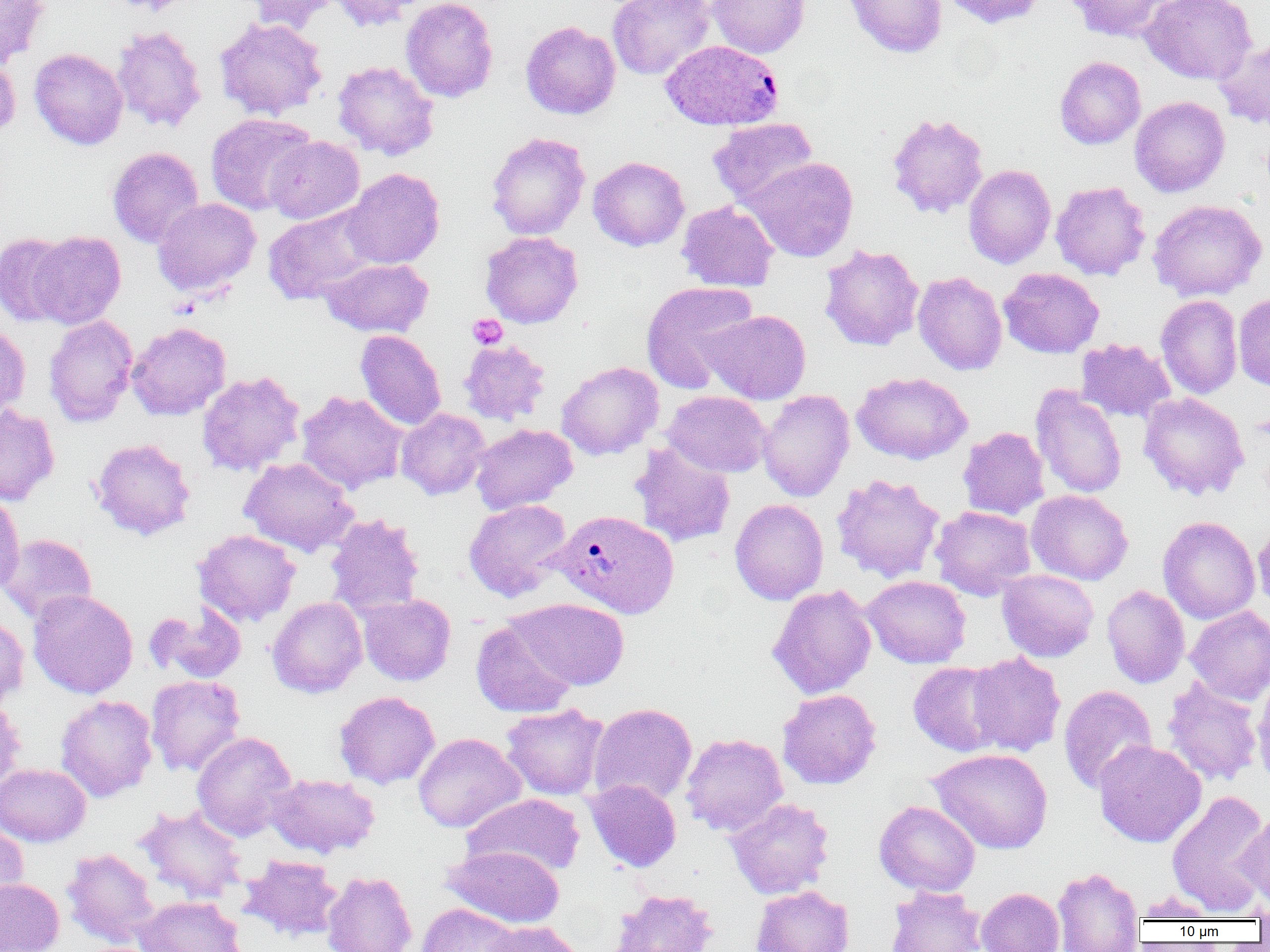
Approximate bounding boxes as named x1/y1/x2/y2 corners in pixels. Uninfected red blood cell locations: (x1=0, y1=0, x2=49, y2=67), (x1=108, y1=0, x2=196, y2=15), (x1=239, y1=0, x2=343, y2=33), (x1=327, y1=0, x2=424, y2=31), (x1=401, y1=0, x2=498, y2=103), (x1=607, y1=0, x2=715, y2=80), (x1=707, y1=0, x2=810, y2=58), (x1=843, y1=0, x2=947, y2=58), (x1=940, y1=0, x2=1047, y2=29), (x1=1064, y1=0, x2=1177, y2=42), (x1=1140, y1=0, x2=1257, y2=85), (x1=214, y1=17, x2=328, y2=120), (x1=520, y1=21, x2=621, y2=119), (x1=112, y1=25, x2=207, y2=133), (x1=1212, y1=36, x2=1270, y2=130), (x1=29, y1=48, x2=128, y2=150), (x1=0, y1=52, x2=20, y2=140), (x1=1054, y1=56, x2=1145, y2=149), (x1=332, y1=60, x2=439, y2=160), (x1=1129, y1=96, x2=1230, y2=197), (x1=886, y1=112, x2=989, y2=218), (x1=205, y1=113, x2=316, y2=216), (x1=708, y1=118, x2=818, y2=207), (x1=486, y1=132, x2=590, y2=240), (x1=265, y1=136, x2=364, y2=224), (x1=107, y1=147, x2=205, y2=248), (x1=588, y1=156, x2=689, y2=251), (x1=742, y1=157, x2=859, y2=262), (x1=963, y1=164, x2=1056, y2=268), (x1=342, y1=168, x2=444, y2=269), (x1=1051, y1=181, x2=1151, y2=280), (x1=153, y1=198, x2=261, y2=296), (x1=668, y1=199, x2=770, y2=388), (x1=1148, y1=199, x2=1267, y2=301), (x1=676, y1=200, x2=779, y2=292), (x1=263, y1=204, x2=381, y2=304), (x1=26, y1=230, x2=126, y2=328), (x1=480, y1=231, x2=584, y2=328), (x1=0, y1=232, x2=74, y2=327), (x1=819, y1=244, x2=924, y2=351), (x1=320, y1=258, x2=433, y2=337), (x1=998, y1=267, x2=1104, y2=358), (x1=912, y1=271, x2=1007, y2=375), (x1=641, y1=281, x2=758, y2=392), (x1=1233, y1=293, x2=1270, y2=392), (x1=1156, y1=294, x2=1243, y2=399), (x1=704, y1=309, x2=811, y2=404), (x1=44, y1=315, x2=138, y2=427), (x1=0, y1=322, x2=30, y2=421), (x1=127, y1=322, x2=231, y2=420), (x1=355, y1=330, x2=446, y2=431), (x1=1076, y1=338, x2=1175, y2=423), (x1=458, y1=339, x2=550, y2=425), (x1=556, y1=361, x2=664, y2=460), (x1=197, y1=371, x2=305, y2=475), (x1=852, y1=372, x2=972, y2=465), (x1=1030, y1=384, x2=1127, y2=498), (x1=758, y1=389, x2=855, y2=502), (x1=296, y1=390, x2=408, y2=494), (x1=663, y1=390, x2=771, y2=477), (x1=1139, y1=392, x2=1249, y2=500), (x1=0, y1=404, x2=59, y2=505), (x1=396, y1=408, x2=490, y2=500), (x1=470, y1=423, x2=577, y2=514), (x1=957, y1=427, x2=1050, y2=520), (x1=91, y1=438, x2=196, y2=541), (x1=630, y1=442, x2=737, y2=548), (x1=239, y1=457, x2=359, y2=557), (x1=830, y1=473, x2=946, y2=583), (x1=1026, y1=489, x2=1133, y2=585), (x1=0, y1=490, x2=25, y2=596), (x1=730, y1=498, x2=828, y2=605), (x1=463, y1=499, x2=573, y2=602), (x1=930, y1=506, x2=1036, y2=600), (x1=325, y1=514, x2=425, y2=616), (x1=1158, y1=516, x2=1261, y2=624), (x1=1253, y1=523, x2=1270, y2=614), (x1=193, y1=529, x2=301, y2=627), (x1=0, y1=533, x2=97, y2=624), (x1=997, y1=569, x2=1098, y2=662), (x1=862, y1=575, x2=971, y2=668), (x1=767, y1=585, x2=877, y2=699), (x1=1101, y1=585, x2=1190, y2=688), (x1=27, y1=590, x2=138, y2=699), (x1=358, y1=593, x2=456, y2=685), (x1=267, y1=596, x2=367, y2=698), (x1=509, y1=598, x2=630, y2=690), (x1=147, y1=603, x2=247, y2=683), (x1=1186, y1=605, x2=1270, y2=704), (x1=0, y1=614, x2=30, y2=708), (x1=471, y1=620, x2=578, y2=718), (x1=964, y1=652, x2=1066, y2=757), (x1=908, y1=661, x2=1008, y2=757), (x1=146, y1=675, x2=245, y2=776), (x1=1161, y1=676, x2=1264, y2=787), (x1=1252, y1=678, x2=1270, y2=789), (x1=1058, y1=684, x2=1158, y2=795), (x1=777, y1=689, x2=882, y2=789), (x1=334, y1=691, x2=440, y2=789), (x1=55, y1=694, x2=157, y2=802), (x1=0, y1=696, x2=26, y2=794), (x1=500, y1=703, x2=609, y2=800), (x1=588, y1=703, x2=697, y2=806), (x1=192, y1=731, x2=297, y2=841), (x1=413, y1=732, x2=526, y2=833), (x1=680, y1=733, x2=788, y2=836), (x1=1094, y1=739, x2=1207, y2=848), (x1=927, y1=747, x2=1053, y2=854), (x1=0, y1=763, x2=91, y2=847), (x1=266, y1=773, x2=380, y2=858), (x1=584, y1=779, x2=682, y2=872), (x1=1166, y1=789, x2=1270, y2=915), (x1=463, y1=792, x2=584, y2=879), (x1=725, y1=798, x2=834, y2=899), (x1=874, y1=800, x2=980, y2=896), (x1=135, y1=804, x2=248, y2=903), (x1=1238, y1=807, x2=1270, y2=912), (x1=0, y1=823, x2=28, y2=914), (x1=444, y1=844, x2=565, y2=929), (x1=61, y1=848, x2=159, y2=948), (x1=238, y1=854, x2=344, y2=942), (x1=1052, y1=866, x2=1145, y2=952), (x1=321, y1=870, x2=417, y2=952), (x1=0, y1=878, x2=64, y2=952), (x1=751, y1=885, x2=854, y2=952), (x1=886, y1=886, x2=986, y2=952), (x1=976, y1=887, x2=1064, y2=952), (x1=609, y1=888, x2=718, y2=952), (x1=1133, y1=892, x2=1220, y2=922), (x1=132, y1=895, x2=246, y2=952), (x1=1245, y1=897, x2=1270, y2=923), (x1=417, y1=903, x2=520, y2=952), (x1=481, y1=921, x2=583, y2=952). Plasmodium vivax-infected red blood cell locations: (x1=661, y1=40, x2=784, y2=131), (x1=551, y1=509, x2=679, y2=619). Platelet locations: (x1=467, y1=314, x2=507, y2=350). Slide-level diagnosis: Plasmodium vivax. Thin blood smear. Single field of view. Optical microscopy. Captured at 1000x magnification. Image is 1270×952 pixels.